Give the location of every WBC.
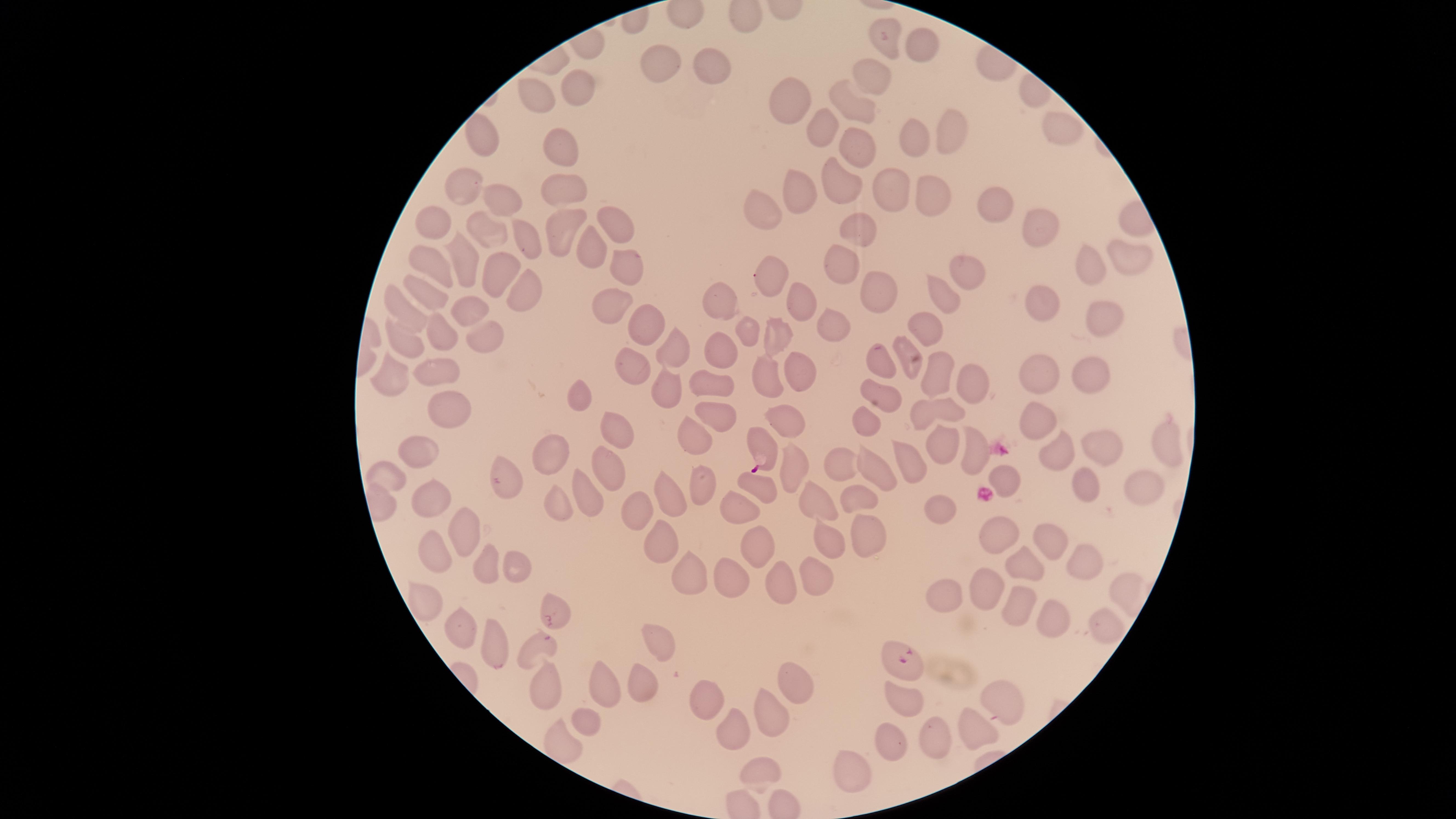
No WBCs identified.

Approximate marker points as {x, y} in pixels. Parasitized RBCs: {763, 444}, {555, 616}, {895, 659}. Uninfected RBCs: {885, 38}, {923, 43}, {661, 65}, {711, 70}, {871, 73}, {581, 84}, {535, 97}, {791, 105}, {854, 110}, {823, 127}, {1060, 127}, {950, 129}, {483, 136}, {915, 136}, {560, 137}, {857, 143}, {465, 181}, {836, 181}, {803, 185}, {567, 187}, {891, 188}, {926, 196}, {502, 200}, {989, 202}, {765, 211}, {611, 225}, {1044, 229}, {559, 230}, {868, 231}, {481, 235}, {525, 238}, {595, 249}, {1130, 252}, {459, 261}, {433, 264}, {1092, 266}, {843, 267}, {627, 271}, {965, 271}, {769, 274}, {496, 279}, {430, 289}, {880, 290}, {525, 292}, {792, 298}, {940, 298}, {721, 301}, {1044, 301}, {611, 302}, {471, 308}, {406, 309}, {1103, 321}, {825, 323}, {645, 325}, {926, 327}, {441, 331}, {749, 331}, {776, 337}, {481, 338}, {405, 339}, {670, 348}, {725, 351}, {908, 356}, {886, 358}, {632, 365}, {936, 368}, {801, 369}, {433, 371}, {1034, 371}, {769, 372}, {1086, 372}, {968, 377}, {389, 380}, {663, 386}, {714, 386}, {890, 393}, {579, 395}, {948, 411}, {444, 414}, {1040, 415}, {790, 416}, {869, 418}, {716, 420}, {615, 428}, {692, 439}, {1103, 443}, {944, 444}, {1163, 445}, {553, 449}, {1056, 452}, {419, 453}, {839, 466}, {797, 467}, {907, 468}, {608, 469}, {873, 474}, {506, 477}, {1006, 477}, {389, 481}, {1143, 484}, {1086, 485}, {759, 487}, {700, 488}, {587, 491}, {671, 495}, {431, 496}, {856, 499}, {553, 502}, {819, 504}, {938, 505}, {739, 509}, {636, 511}, {463, 525}, {998, 534}, {867, 539}, {828, 540}, {1051, 540}, {753, 544}, {654, 546}, {434, 556}, {1031, 560}, {485, 564}, {1086, 565}, {515, 566}, {811, 573}, {731, 577}, {684, 578}, {777, 582}, {982, 588}, {945, 594}, {423, 602}, {1016, 606}, {1056, 621}, {462, 627}, {1102, 631}, {495, 643}, {653, 643}, {536, 648}, {791, 672}, {639, 677}, {546, 684}, {602, 684}, {909, 698}, {1006, 698}, {707, 699}, {772, 710}, {587, 719}, {735, 727}, {975, 727}, {931, 735}, {890, 739}, {856, 766}, {762, 775}. Image is 1456×819 pixels. The visible region is circular. Thin smear of blood. Presence: malaria parasites seen. Giemsa-stained preparation. Single field of view. Photographed with a smartphone camera through the microscope eyepiece. Species: Plasmodium falciparum.